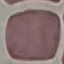
Summary:
  - Result: no malaria parasites seen
  - Image type: cell patch, automatically extracted from a larger field of view and resized to 64 × 64 pixels
  - Stain: Giemsa
  - Capture: smartphone camera at the microscope eyepiece
  - Preparation: thin smear